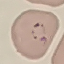 Result: malaria parasites identified. Acquired by smartphone through the microscope eyepiece. Thin smear of blood. Giemsa stain. Automatically extracted cell patch, resized to 64 × 64 pixels.